Classify the preparation.
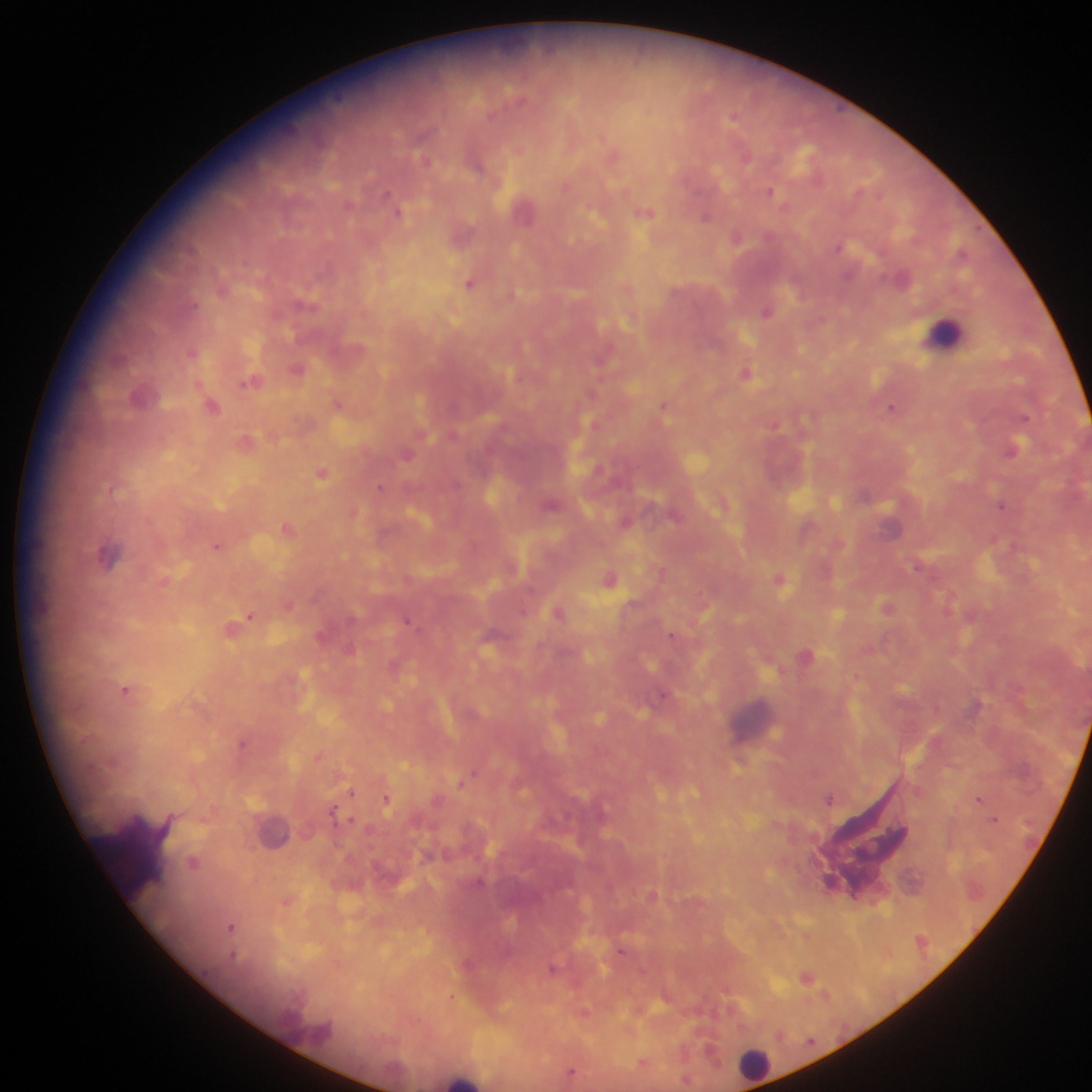

This is a thick smear.

Approximate centers as (x, y) in pixels.
Summary:
  - Malaria parasite locations: (770, 190), (785, 206), (647, 213), (737, 236), (838, 248), (471, 282), (768, 310), (191, 351), (296, 367), (747, 372), (250, 380), (337, 401), (664, 404), (213, 405), (894, 405), (1025, 417), (245, 440), (1013, 447), (322, 472), (111, 488), (380, 488), (1002, 505), (287, 527), (216, 545), (610, 577), (781, 579), (289, 605), (888, 605), (558, 611), (252, 616), (406, 619), (231, 628), (671, 635), (125, 689), (1021, 691), (940, 704), (243, 744), (319, 756), (475, 772), (459, 784), (351, 792), (387, 798), (831, 798), (979, 799), (333, 807), (350, 820), (194, 862), (287, 904), (231, 927), (554, 967), (808, 976), (728, 991), (451, 997), (583, 1011)
  - Leukocyte locations: (946, 334), (756, 1066)
  - Field of view: single
  - Capture: mobile-phone photograph through a microscope
  - Country: Ghana
  - Image size: 1092×1092 pixels